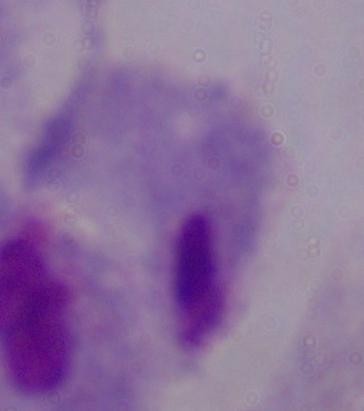
A trichomonad is shown. Captured at 1000x magnification. Photomicrograph.